Name the cell type shown.
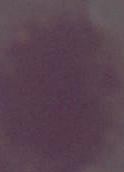

This is an erythrocyte.

Summary:
  - Magnification: 1000x
  - Modality: photomicrograph